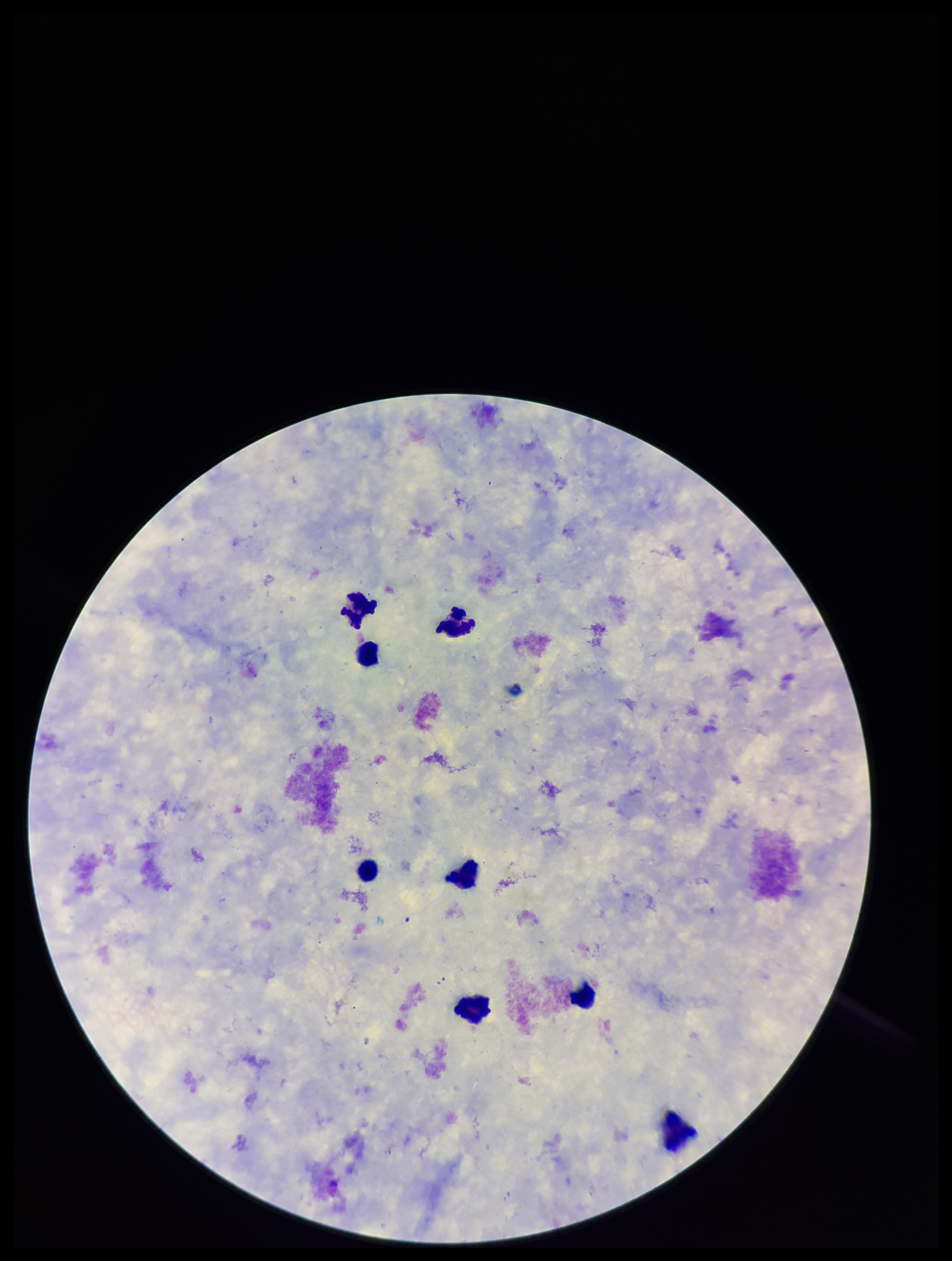
Leukocyte count: 8. Plasmodium parasites: none detected. Giemsa stain. One field from this slide. Parasite count: 0. Patient malaria status: negative. Preparation: thick. Smartphone photograph taken through the eyepiece of a microscope. Image is 952×1261 pixels.